Classify this cell by malaria status.
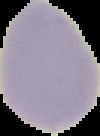

Uninfected.

Summary:
  - Image type: cell region segmented out of the field of view; surrounding area masked to black
  - Image size: 100×136 pixels
  - Preparation: thin blood smear